Classify this cell by malaria status.
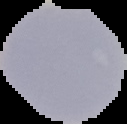
Uninfected.

image type = cell region segmented out of the field of view; surrounding area masked to black
image size = 127×124 pixels
preparation = thin blood smear